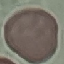

result: no malaria parasites seen
capture: smartphone through the microscope eyepiece
preparation: thin blood smear
image_type: cell patch, automatically extracted from a larger field of view and resized to 64 × 64 pixels
stain: Giemsa